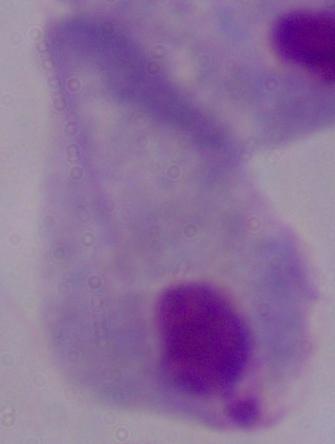

1000x magnification. Micrograph. A trichomonad is seen.